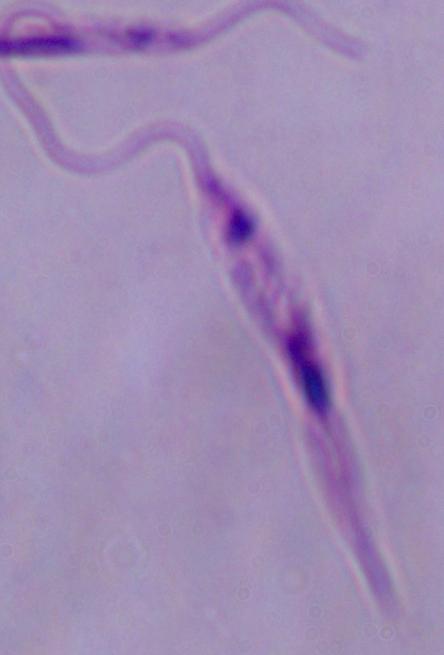

Summary:
  - Magnification: 1000x
  - Identification: Leishmania
  - Modality: photomicrograph